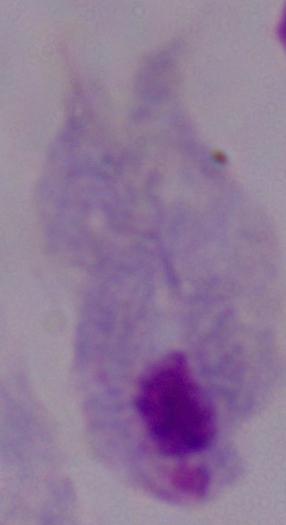 Micrograph. A trichomonad is shown. Captured at 1000x magnification.